Assess the morphology of the erythrocytes.
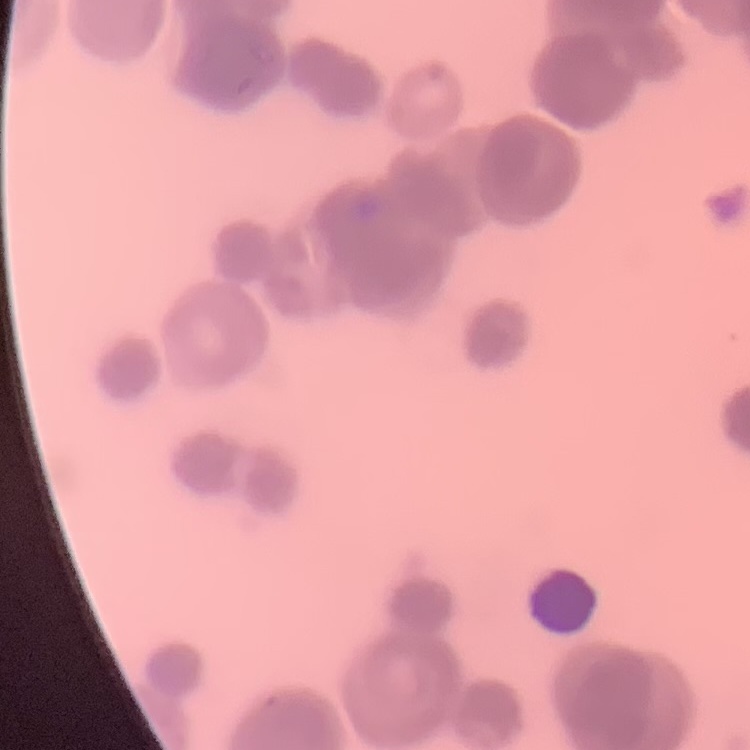
They show rouleaux formation.

stain: Field's or Giemsa
image_type: square crop of a larger photomicrograph
preparation: thin blood smear